Locate every blood parasite and identify its species.
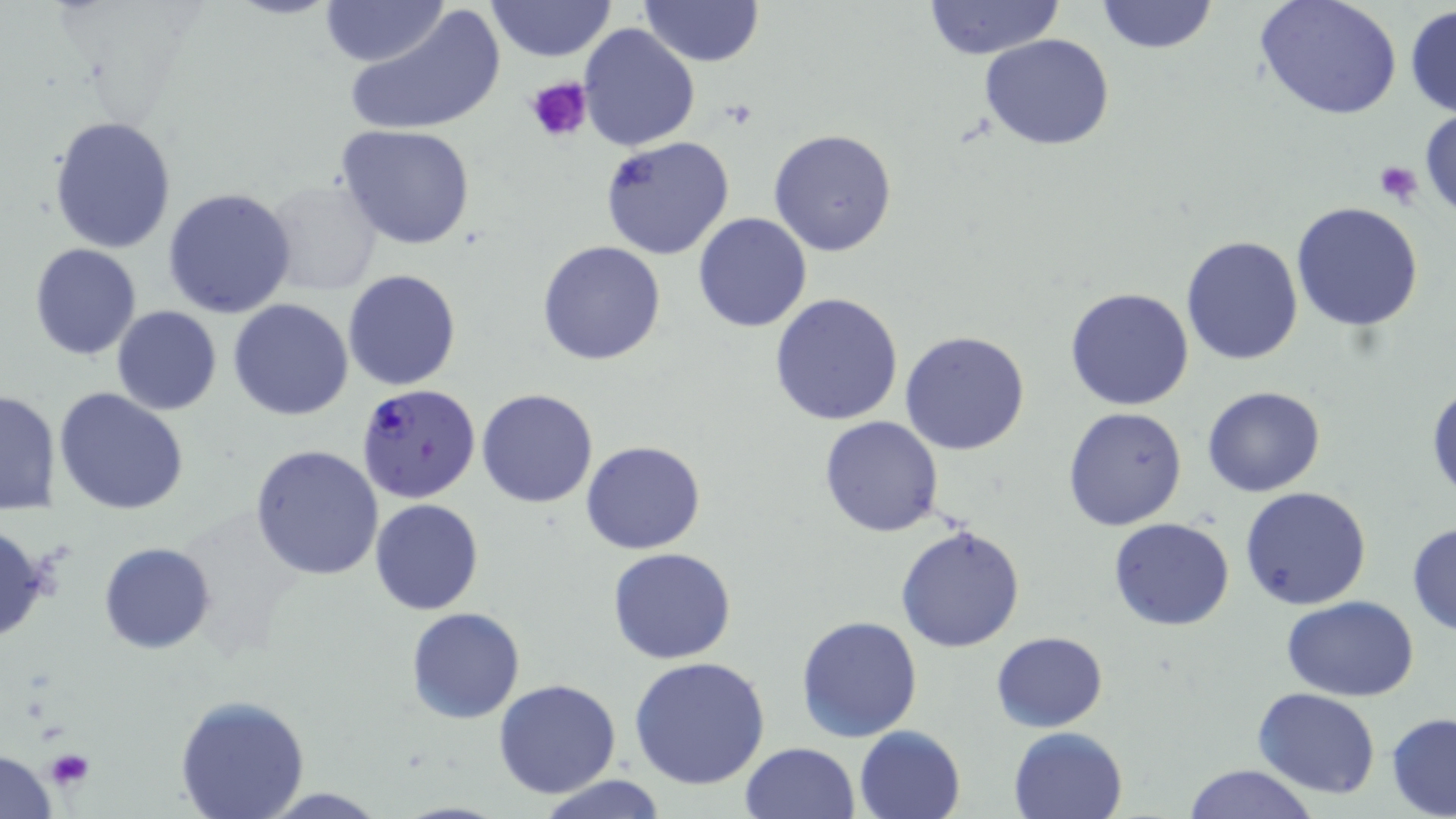
Approximate bounding boxes as [x1, y1, x2, y2] in pixels.
Plasmodium falciparum-infected red blood cells: [356, 383, 484, 504].
No Plasmodium ovale, Plasmodium malariae, Plasmodium vivax, Babesia divergens, or Trypanosoma brucei observed.

Uninfected red blood cell locations (subset): [322, 0, 448, 67], [486, 0, 617, 63], [638, 0, 764, 68], [1097, 0, 1217, 55], [1254, 0, 1403, 122], [922, 1, 1063, 60], [1405, 5, 1456, 117], [345, 6, 504, 138], [578, 23, 702, 152], [980, 33, 1114, 151], [1418, 107, 1456, 221], [48, 115, 178, 254], [335, 124, 478, 250], [768, 129, 897, 257], [600, 135, 735, 261], [261, 178, 384, 295], [162, 187, 298, 319], [1291, 202, 1425, 332], [692, 212, 813, 331], [1182, 235, 1304, 366], [537, 240, 666, 365], [29, 244, 142, 362], [343, 268, 462, 392], [1064, 287, 1195, 411], [770, 293, 905, 427], [227, 299, 354, 420], [110, 305, 222, 415], [899, 330, 1030, 456], [1427, 384, 1456, 500], [1202, 385, 1325, 497], [54, 387, 190, 516], [477, 389, 599, 509], [1, 390, 62, 516], [1062, 406, 1188, 532], [819, 416, 944, 537], [581, 440, 706, 555], [250, 443, 385, 580], [1239, 487, 1372, 611], [370, 498, 484, 617], [1109, 518, 1235, 632], [0, 520, 50, 650], [1406, 521, 1456, 635], [895, 522, 1025, 651], [98, 542, 217, 654], [608, 547, 737, 664], [1283, 595, 1421, 701], [406, 607, 526, 725], [796, 615, 923, 742], [991, 631, 1109, 732], [628, 658, 772, 791], [493, 679, 621, 800], [1253, 687, 1382, 799], [174, 695, 310, 817], [1386, 712, 1456, 818], [1008, 725, 1129, 819], [853, 728, 965, 819], [738, 742, 860, 819], [1181, 763, 1315, 819], [533, 774, 670, 818], [255, 787, 391, 817]. Platelet locations (subset): [526, 76, 591, 145], [1374, 161, 1424, 207], [43, 749, 95, 791]. Slide-level diagnosis: Plasmodium falciparum. Thin blood smear. May-Grünwald-Giemsa-stained preparation. 1000x magnification. One field of a larger specimen. Optical microscopy. Image is 1456×819 pixels.